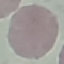

Result: no malaria parasites detected. Giemsa stain. Cell patch, automatically extracted from a larger field of view and resized to 64 × 64 pixels. Photographed with a smartphone camera at the microscope eyepiece. Thin smear of blood.